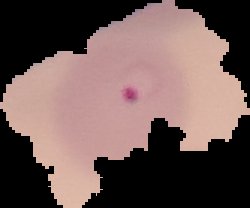
Image is 250×208 pixels. Result: Plasmodium parasites identified. The area outside the segmented cell region is set to black. From a thin blood film.